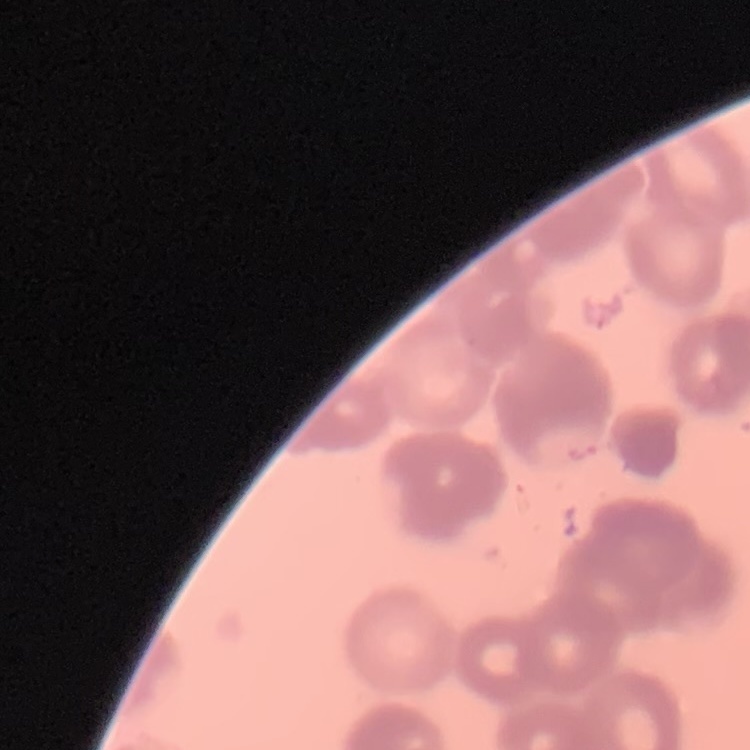
Summary:
  - Erythrocyte morphology: rouleaux formation
  - Preparation: thin peripheral smear
  - Stain: Field's or Giemsa
  - Image type: one tile cut from a larger photomicrograph